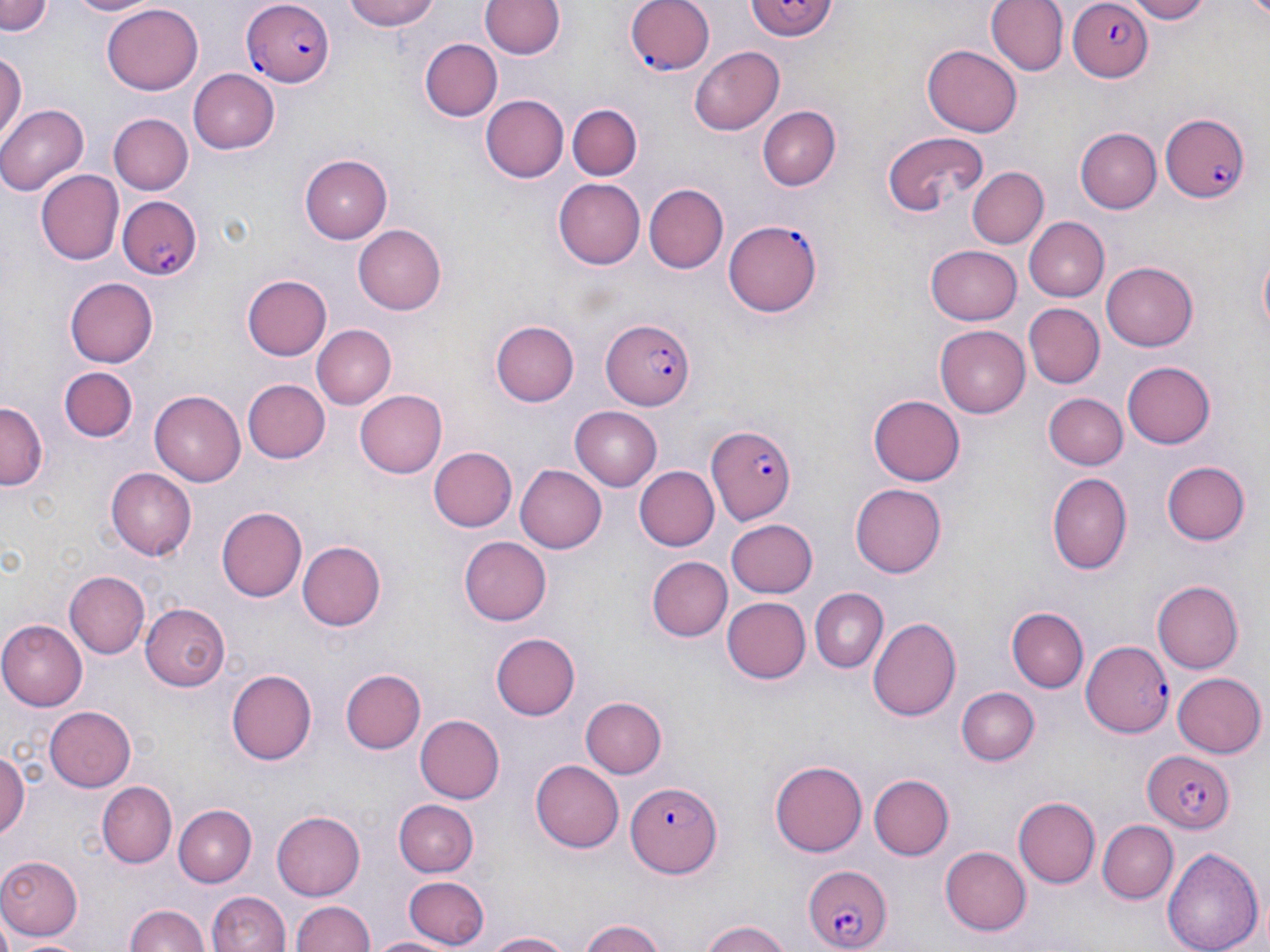
{
  "slide_level_diagnosis": "Plasmodium falciparum",
  "field_of_view": "one of a larger specimen",
  "preparation": "thin blood film",
  "image_size": "1270×952 pixels",
  "modality": "light microscopy",
  "stain": "May-Grünwald-Giemsa",
  "plasmodium_falciparum_infected_red_blood_cell_locations": "approximate bounding boxes as named x1/y1/x2/y2 corners in pixels: (x1=241, y1=0, x2=333, y2=86), (x1=628, y1=0, x2=716, y2=77), (x1=743, y1=0, x2=840, y2=42), (x1=1068, y1=1, x2=1152, y2=80), (x1=1158, y1=109, x2=1253, y2=205), (x1=117, y1=195, x2=204, y2=281), (x1=723, y1=220, x2=821, y2=317), (x1=599, y1=319, x2=696, y2=410), (x1=708, y1=425, x2=798, y2=524), (x1=1085, y1=640, x2=1174, y2=740), (x1=1143, y1=749, x2=1235, y2=834), (x1=625, y1=779, x2=724, y2=874), (x1=801, y1=864, x2=893, y2=951)",
  "magnification": "1000x",
  "uninfected_red_blood_cell_locations": "approximate bounding boxes as named x1/y1/x2/y2 corners in pixels: (x1=1, y1=0, x2=55, y2=37), (x1=68, y1=0, x2=161, y2=18), (x1=339, y1=0, x2=447, y2=30), (x1=985, y1=0, x2=1065, y2=76), (x1=1122, y1=0, x2=1213, y2=23), (x1=481, y1=1, x2=564, y2=60), (x1=103, y1=2, x2=202, y2=91), (x1=420, y1=40, x2=501, y2=121), (x1=689, y1=46, x2=783, y2=134), (x1=922, y1=46, x2=1023, y2=136), (x1=0, y1=51, x2=26, y2=143), (x1=187, y1=68, x2=278, y2=154), (x1=483, y1=95, x2=569, y2=182), (x1=567, y1=102, x2=642, y2=180), (x1=0, y1=105, x2=86, y2=196), (x1=758, y1=106, x2=840, y2=189), (x1=107, y1=113, x2=193, y2=195), (x1=1074, y1=128, x2=1162, y2=214), (x1=879, y1=130, x2=991, y2=216), (x1=298, y1=153, x2=392, y2=245), (x1=967, y1=166, x2=1048, y2=249), (x1=38, y1=170, x2=124, y2=264), (x1=553, y1=178, x2=646, y2=269), (x1=647, y1=184, x2=727, y2=272), (x1=1026, y1=219, x2=1109, y2=300), (x1=353, y1=224, x2=450, y2=316), (x1=928, y1=242, x2=1023, y2=322), (x1=1102, y1=262, x2=1198, y2=350), (x1=239, y1=270, x2=335, y2=361), (x1=65, y1=279, x2=158, y2=367), (x1=1024, y1=304, x2=1104, y2=388), (x1=490, y1=320, x2=579, y2=408), (x1=313, y1=324, x2=395, y2=407), (x1=936, y1=324, x2=1033, y2=417), (x1=1120, y1=360, x2=1215, y2=449), (x1=60, y1=367, x2=138, y2=443), (x1=241, y1=378, x2=329, y2=464), (x1=356, y1=390, x2=447, y2=478), (x1=150, y1=391, x2=244, y2=486), (x1=1043, y1=392, x2=1127, y2=470), (x1=868, y1=395, x2=965, y2=485), (x1=0, y1=400, x2=47, y2=487), (x1=570, y1=405, x2=663, y2=491), (x1=427, y1=447, x2=516, y2=533), (x1=1160, y1=460, x2=1249, y2=545), (x1=517, y1=464, x2=607, y2=553), (x1=633, y1=466, x2=717, y2=552), (x1=105, y1=467, x2=197, y2=560), (x1=1047, y1=472, x2=1131, y2=573), (x1=850, y1=483, x2=944, y2=578), (x1=216, y1=504, x2=306, y2=599), (x1=726, y1=518, x2=818, y2=597), (x1=457, y1=535, x2=551, y2=628), (x1=297, y1=540, x2=385, y2=630), (x1=646, y1=556, x2=731, y2=642), (x1=64, y1=571, x2=148, y2=659), (x1=1152, y1=581, x2=1243, y2=674), (x1=808, y1=588, x2=889, y2=673), (x1=722, y1=597, x2=811, y2=684), (x1=141, y1=603, x2=229, y2=690), (x1=1006, y1=605, x2=1088, y2=691), (x1=867, y1=616, x2=961, y2=720), (x1=0, y1=620, x2=89, y2=709), (x1=490, y1=632, x2=581, y2=720), (x1=226, y1=668, x2=318, y2=766), (x1=341, y1=668, x2=425, y2=753), (x1=1173, y1=673, x2=1265, y2=758), (x1=957, y1=686, x2=1039, y2=766), (x1=581, y1=697, x2=668, y2=777), (x1=44, y1=706, x2=137, y2=792), (x1=414, y1=715, x2=505, y2=803), (x1=0, y1=751, x2=28, y2=840), (x1=770, y1=757, x2=866, y2=854), (x1=530, y1=758, x2=624, y2=853), (x1=870, y1=773, x2=954, y2=859), (x1=96, y1=782, x2=176, y2=867), (x1=1012, y1=796, x2=1098, y2=887), (x1=394, y1=799, x2=478, y2=874), (x1=175, y1=803, x2=256, y2=887), (x1=271, y1=810, x2=366, y2=901), (x1=1097, y1=820, x2=1178, y2=902), (x1=1163, y1=842, x2=1263, y2=952), (x1=940, y1=847, x2=1032, y2=937), (x1=0, y1=856, x2=82, y2=941), (x1=405, y1=876, x2=488, y2=948), (x1=206, y1=891, x2=289, y2=952), (x1=292, y1=899, x2=375, y2=952), (x1=123, y1=905, x2=212, y2=952), (x1=578, y1=919, x2=668, y2=952), (x1=696, y1=920, x2=795, y2=952), (x1=483, y1=930, x2=578, y2=952), (x1=370, y1=933, x2=457, y2=952), (x1=11, y1=934, x2=95, y2=952)"
}